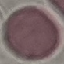
Result: no malaria parasites detected. Giemsa-stained preparation. Thin blood smear. Automatically extracted cell patch, resized to 64 × 64 pixels. Photographed with a smartphone camera at the microscope eyepiece.